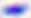
Toxoplasma gondii is shown. 400x magnification. Photomicrograph.